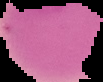
image type = segmented cell region on a black background
image size = 103×82 pixels
preparation = thin blood film
result = negative for Plasmodium parasites